Comment on the morphology of the red blood cells.
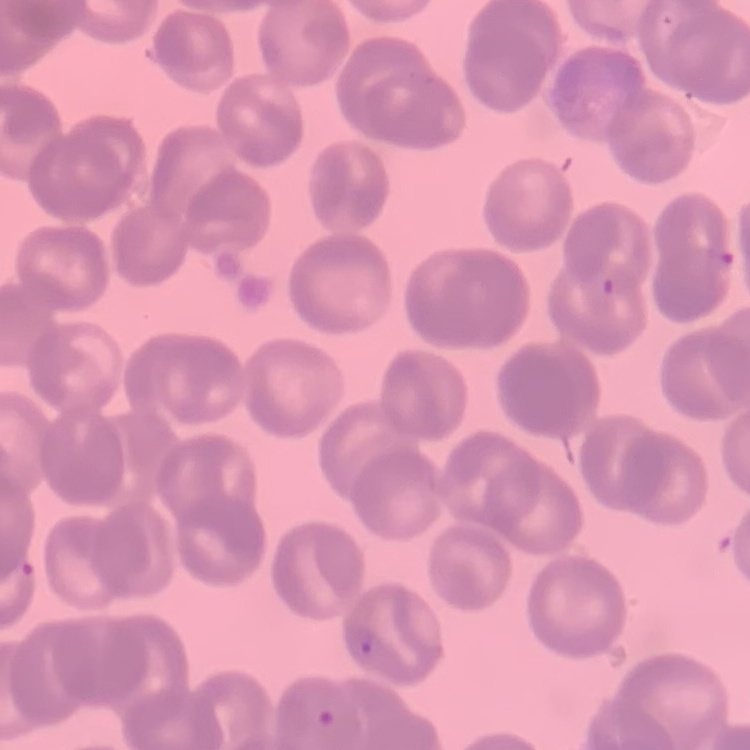
They show rouleaux formation.

Thin peripheral smear. Stained with either Field's or Giemsa. One tile cut from a larger photomicrograph.